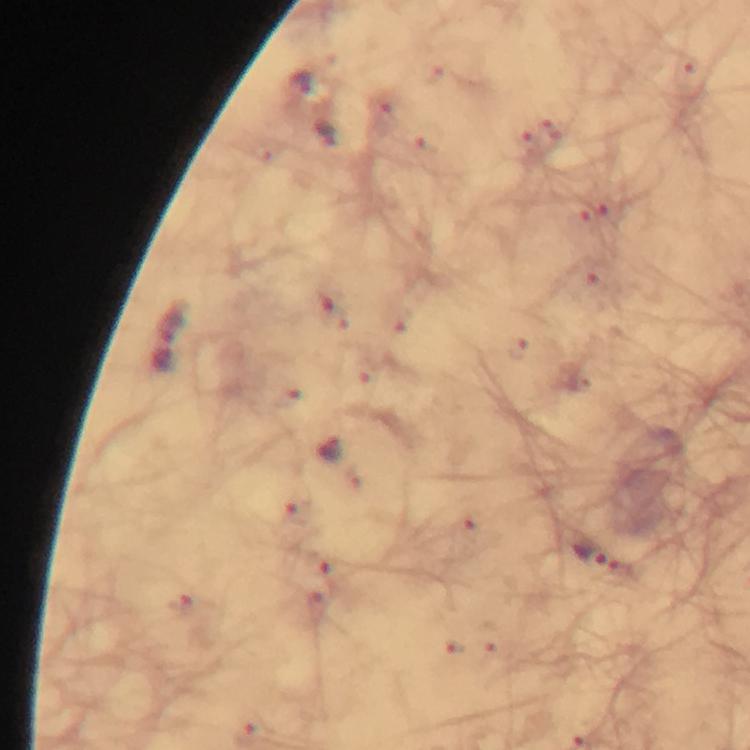

Approximate object centers, in pixels from the top-left corner.
Summary:
  - Malaria parasite locations: (x=299, y=80), (x=327, y=134), (x=329, y=447), (x=589, y=552)
  - Stain: Giemsa
  - Context: from a diagnostic examination for malaria
  - Cropped from: a single field of view
  - Image size: 750×750 pixels
  - Preparation: thick blood film
  - Capture: smartphone camera through the microscope
  - Immersion oil: used
  - Magnification: 100x